Give the position of every P. falciparum parasite, noting its life-cycle stage.
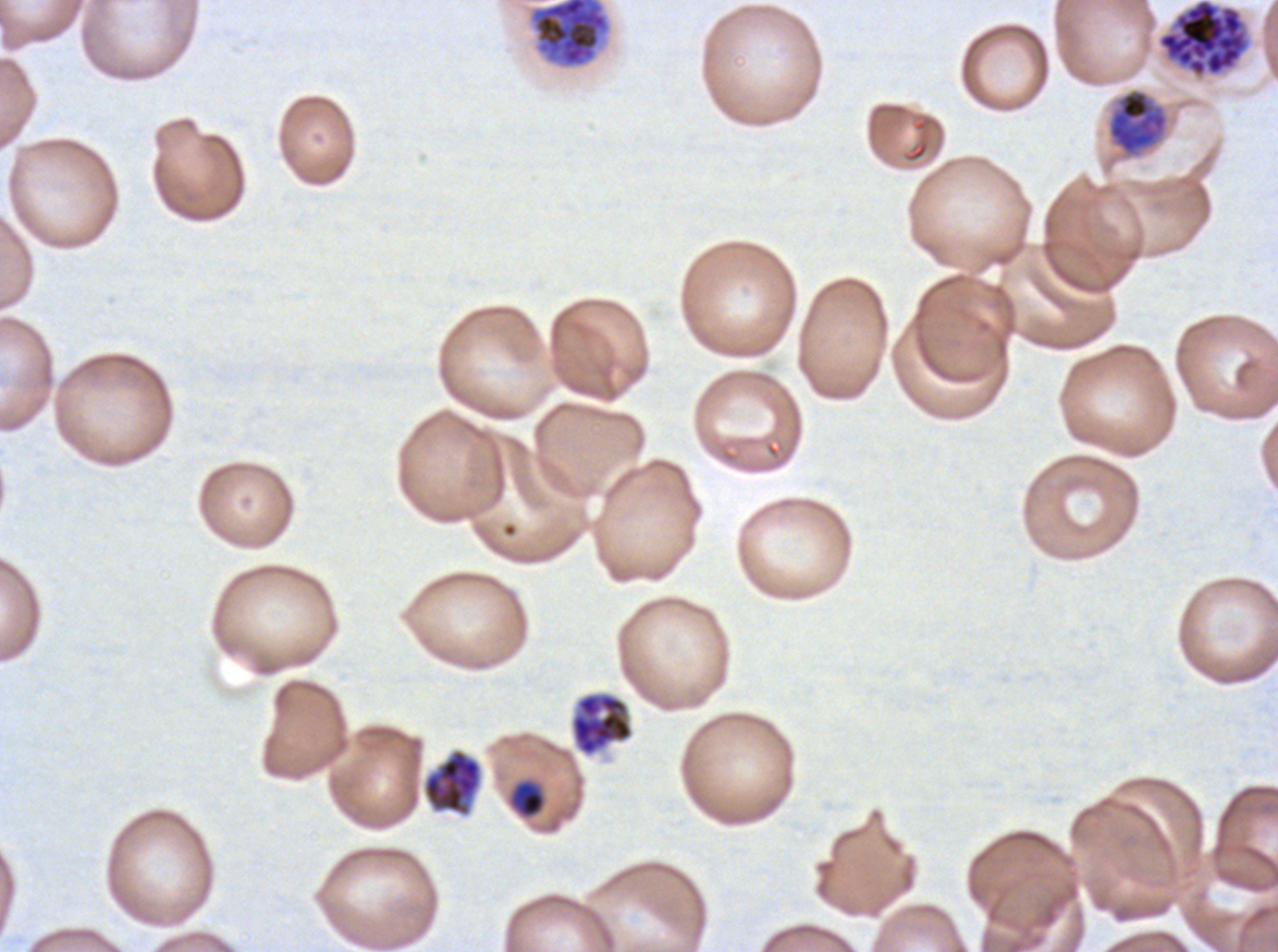
Approximate bounding boxes as (x1, y1, x2, y2) in pixels.
Late-ring/early-trophozoite forms: (510, 780, 546, 818).
Mid trophozoites: (1107, 88, 1169, 157).
Late schizonts: (528, 0, 611, 69).
Segmenters: (1157, 0, 1248, 78), (570, 691, 633, 757), (423, 749, 482, 816).
No rings, late trophozoites, early schizonts, or gametocytes observed.

Summary:
  - Image size: 1278×952 pixels
  - Life-cycle stages observed: late-ring/early-trophozoite, mid trophozoite, late schizont, segmenter
  - Stain: Giemsa
  - Specimen: P. falciparum from a patient in The Gambia, cultured ex vivo for 24 to 48 hours
  - Preparation: thin blood smear
  - Field of view: one sub-image of a larger composite